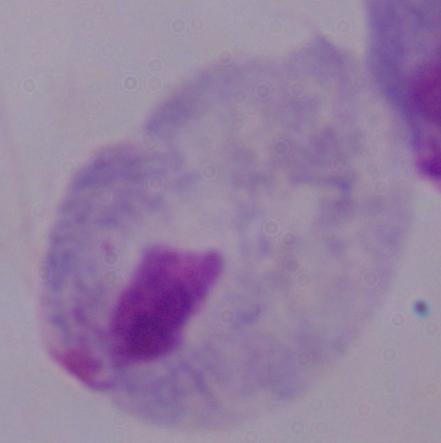

Micrograph. Captured at 1000x magnification. A trichomonad is seen.